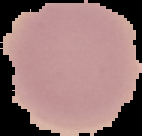
image type = cell region segmented out of the field of view; surrounding area masked to black
preparation = thin blood smear
image size = 142×136 pixels
malaria status = uninfected